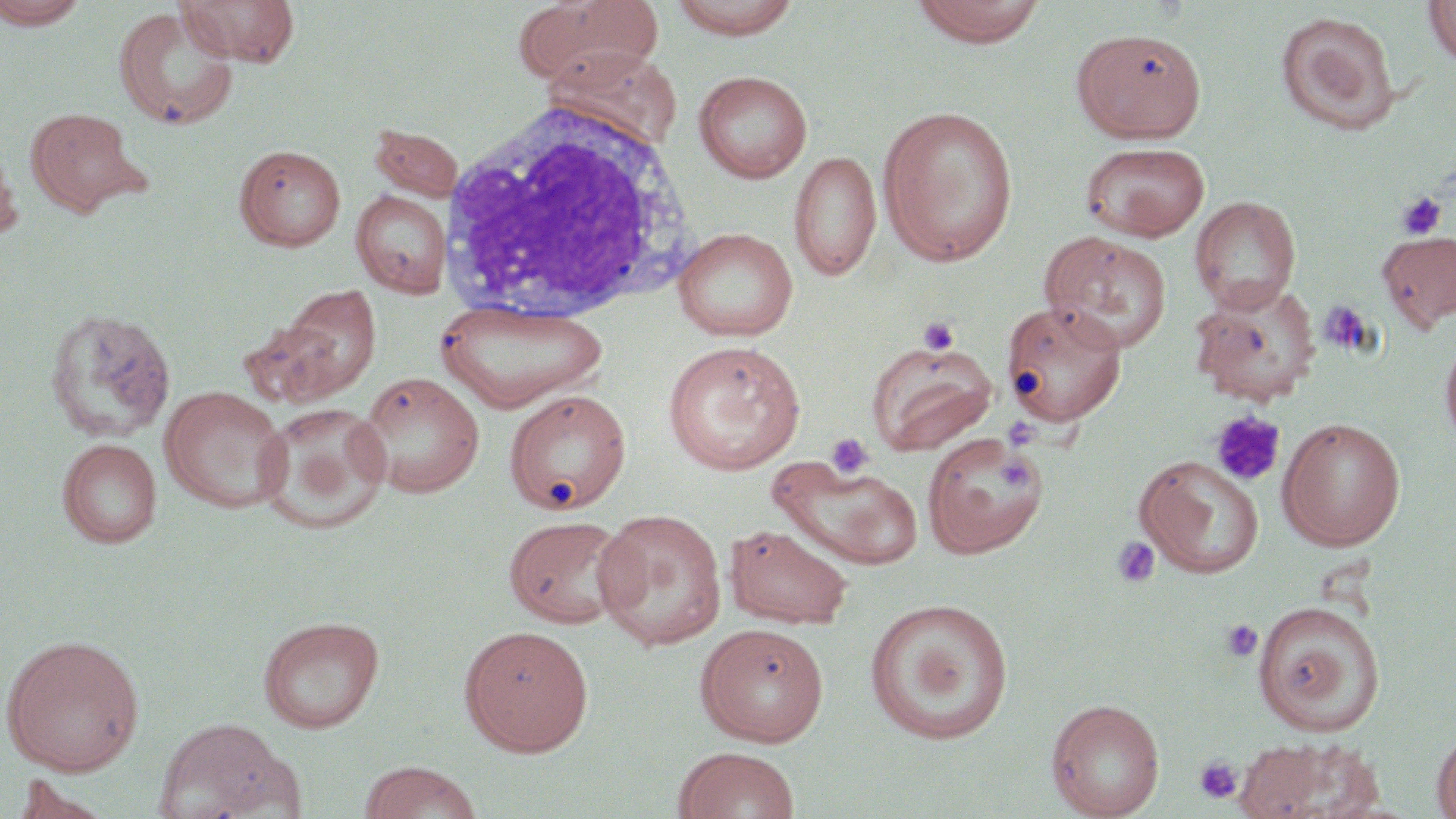

slide-level diagnosis = no evidence of blood parasites
preparation = thin blood film
field of view = single
modality = light microscopy
platelet locations = approximate bounding boxes as named x1/y1/x2/y2 corners in pixels: (x1=1396, y1=191, x2=1447, y2=240), (x1=918, y1=316, x2=960, y2=356), (x1=1209, y1=409, x2=1286, y2=487), (x1=1002, y1=417, x2=1040, y2=451), (x1=825, y1=432, x2=875, y2=480), (x1=997, y1=455, x2=1036, y2=491), (x1=1108, y1=536, x2=1162, y2=588), (x1=1221, y1=619, x2=1263, y2=663), (x1=1194, y1=756, x2=1243, y2=804)
image size = 1456×819 pixels
stain = May-Grünwald-Giemsa
white blood cell locations = approximate bounding boxes as named x1/y1/x2/y2 corners in pixels: (x1=440, y1=99, x2=699, y2=324)
uninfected red blood cell locations = approximate bounding boxes as named x1/y1/x2/y2 corners in pixels: (x1=0, y1=0, x2=90, y2=29), (x1=178, y1=0, x2=300, y2=67), (x1=513, y1=0, x2=665, y2=91), (x1=666, y1=0, x2=805, y2=39), (x1=906, y1=0, x2=1049, y2=48), (x1=1423, y1=0, x2=1456, y2=68), (x1=113, y1=6, x2=240, y2=130), (x1=1275, y1=11, x2=1401, y2=135), (x1=1071, y1=27, x2=1207, y2=143), (x1=544, y1=46, x2=684, y2=151), (x1=693, y1=70, x2=813, y2=183), (x1=878, y1=103, x2=1019, y2=265), (x1=24, y1=106, x2=146, y2=217), (x1=368, y1=123, x2=465, y2=202), (x1=0, y1=141, x2=22, y2=244), (x1=1080, y1=141, x2=1211, y2=241), (x1=234, y1=144, x2=346, y2=251), (x1=789, y1=149, x2=881, y2=283), (x1=351, y1=190, x2=452, y2=297), (x1=1189, y1=195, x2=1301, y2=313), (x1=673, y1=227, x2=798, y2=342), (x1=1040, y1=232, x2=1172, y2=353), (x1=1377, y1=232, x2=1456, y2=331), (x1=1189, y1=281, x2=1322, y2=407), (x1=262, y1=283, x2=382, y2=405), (x1=435, y1=299, x2=608, y2=413), (x1=1000, y1=300, x2=1128, y2=426), (x1=44, y1=307, x2=177, y2=443), (x1=1439, y1=330, x2=1456, y2=451), (x1=661, y1=340, x2=806, y2=475), (x1=865, y1=340, x2=998, y2=456), (x1=358, y1=371, x2=485, y2=498), (x1=160, y1=385, x2=291, y2=513), (x1=504, y1=389, x2=631, y2=515), (x1=256, y1=402, x2=392, y2=534), (x1=1277, y1=417, x2=1406, y2=551), (x1=921, y1=433, x2=1048, y2=559), (x1=57, y1=438, x2=162, y2=548), (x1=1134, y1=454, x2=1265, y2=578), (x1=771, y1=458, x2=924, y2=570), (x1=592, y1=508, x2=727, y2=651), (x1=503, y1=515, x2=632, y2=629), (x1=724, y1=523, x2=854, y2=630), (x1=864, y1=597, x2=1015, y2=744), (x1=1252, y1=600, x2=1386, y2=737), (x1=257, y1=614, x2=385, y2=733), (x1=696, y1=623, x2=830, y2=745), (x1=460, y1=625, x2=594, y2=756), (x1=1, y1=633, x2=145, y2=776), (x1=1046, y1=697, x2=1165, y2=818), (x1=152, y1=717, x2=301, y2=819), (x1=1431, y1=729, x2=1456, y2=819), (x1=1231, y1=737, x2=1382, y2=819), (x1=673, y1=746, x2=801, y2=819), (x1=357, y1=760, x2=483, y2=819)
magnification = 1000x